State the preparation type.
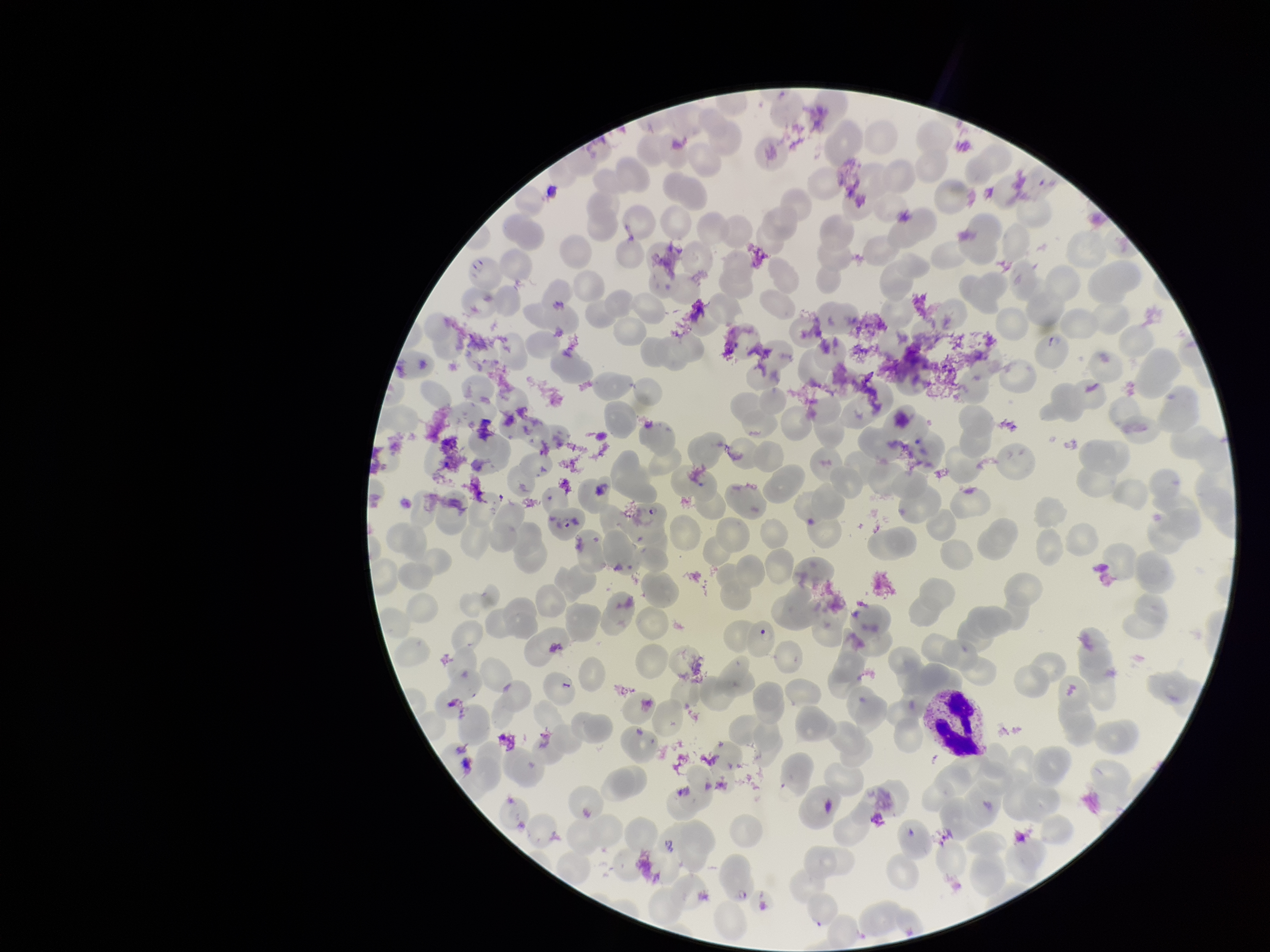
Thin.

Giemsa stain. One field from this slide. Smartphone photograph taken through the eyepiece of a microscope. Parasitized red blood cells: detected. Image is 1270×952 pixels. Parasitized red blood cell count: 4. Patient malaria status: infected. Red blood cell count: 266. Species reported for this patient: Plasmodium falciparum.